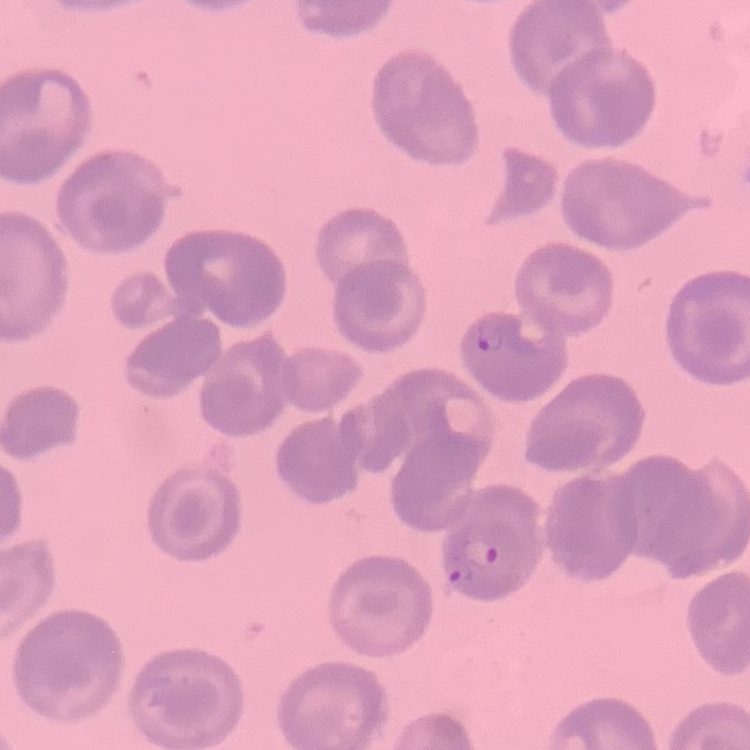

Summary:
  - Red blood cell morphology: no rouleaux formation
  - Stain: Field's or Giemsa
  - Preparation: thin blood film
  - Image type: one tile cut from a larger photomicrograph